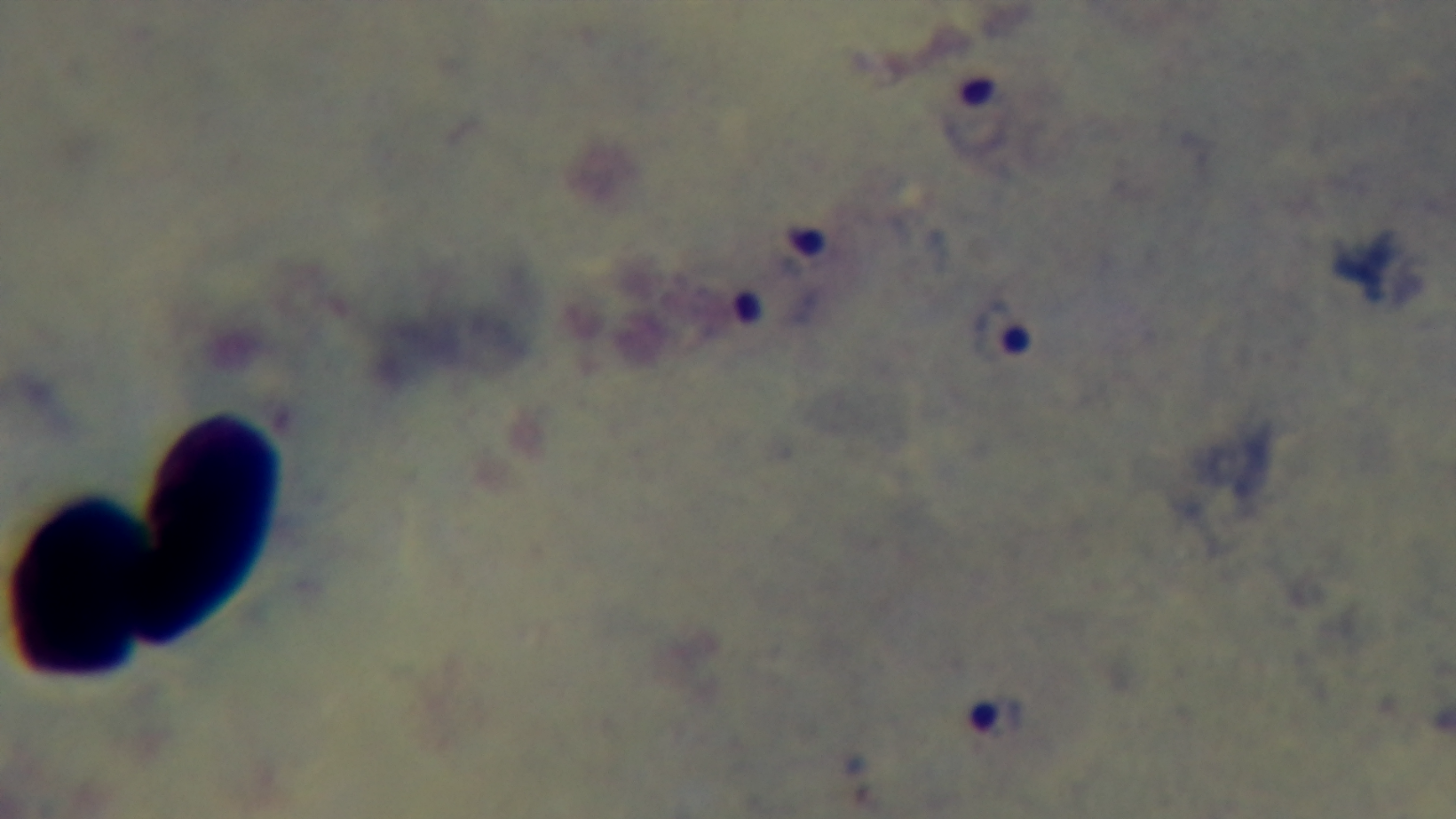
Giemsa stain. Malaria status: positive. Preparation: thick. Captured with a mounted 4K digital camera. Photomicrograph. 100x oil-immersion objective. One field from the slide.